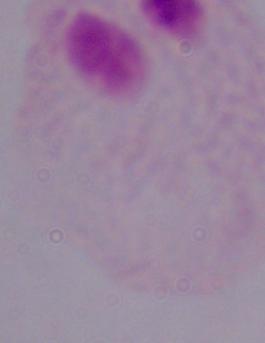
Micrograph. Captured at 1000x magnification. A trichomonad is seen.